Comment on the morphology of the erythrocytes.
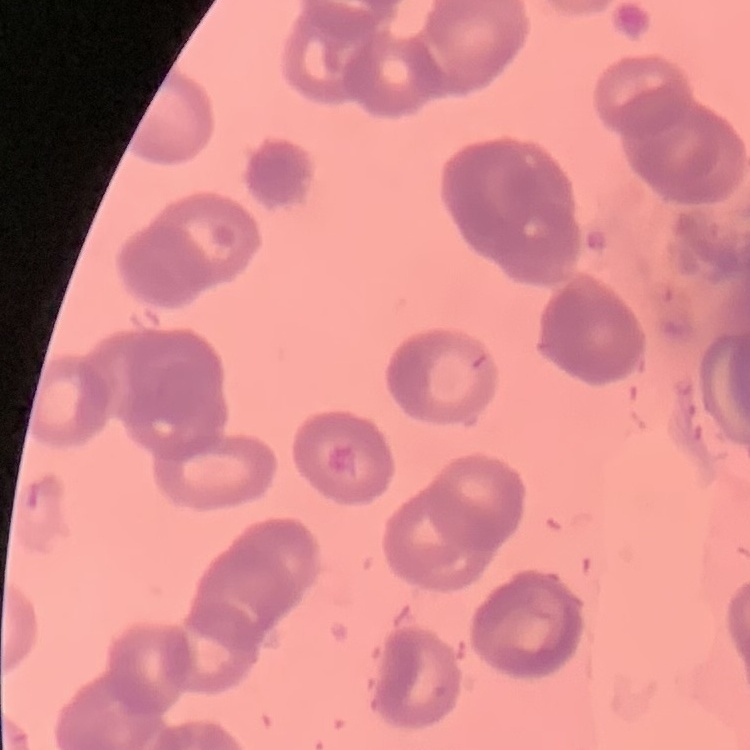

Rouleaux formation.

stain = Field's or Giemsa
preparation = thin blood film
image type = square crop of a larger photomicrograph